State which cell type is depicted.
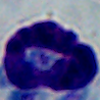

A leukocyte.

magnification = 1000x
modality = photomicrograph